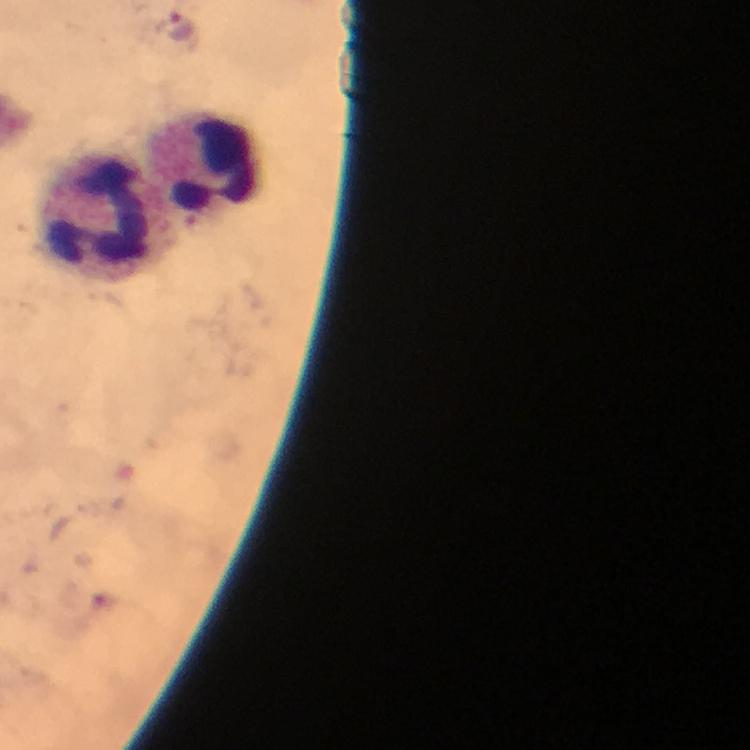 Approximate object centers, in pixels from the top-left corner. Plasmodium parasite locations: (x=181, y=26). Leukocyte locations: (x=198, y=171), (x=104, y=226). Image is 750×750 pixels. Giemsa-stained preparation. Photographed with a smartphone mounted on the microscope. 100x magnification. Thick smear. Immersion oil was used. From a malaria diagnostic workup. A crop from one field of view.